Locate the red blood cells and classify each one as Plasmodium falciparum-infected, uninfected, or of indeterminate infection status.
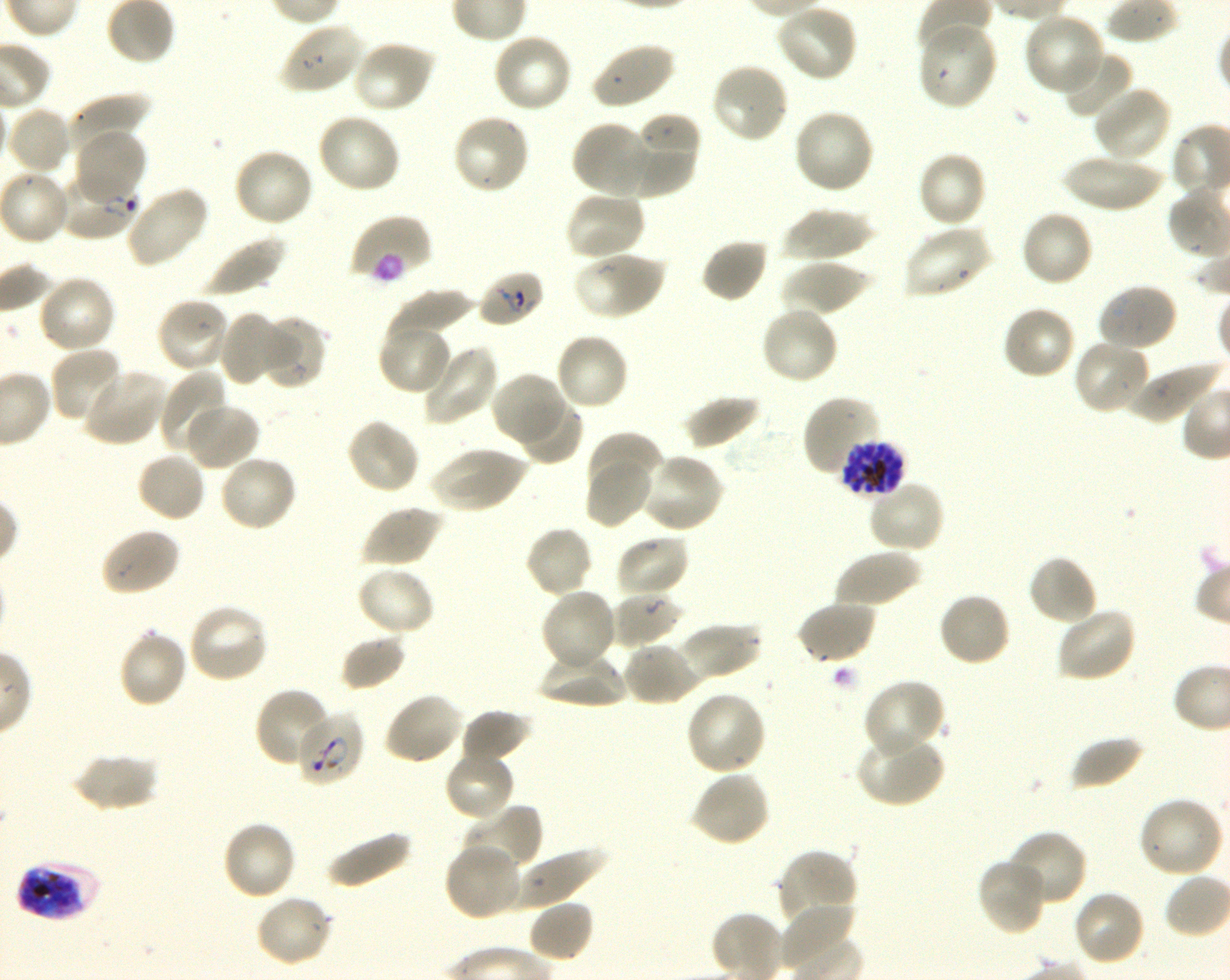

Approximate bounding boxes as (x1, y1, x2, y2) in pixels. Not every red blood cell is marked. A life-cycle stage — or a range of stages, where the recorded stages span more than one — follows each staged infected red blood cell.
Infected red blood cells: (55, 171, 140, 241) ring; (839, 439, 906, 502) schizont; (16, 858, 101, 922) late trophozoite to late schizont.
Red blood cells of indeterminate infection status: (350, 214, 433, 286), (477, 270, 546, 329), (295, 710, 363, 786).
Uninfected red blood cells: (775, 3, 859, 82), (1023, 13, 1107, 96), (280, 21, 366, 96), (917, 21, 998, 111), (491, 32, 573, 114), (352, 39, 435, 114), (590, 41, 675, 110), (1058, 47, 1133, 120), (710, 62, 789, 144), (1093, 84, 1173, 163), (68, 94, 148, 158), (6, 106, 72, 175), (792, 108, 876, 195), (316, 112, 401, 194), (450, 112, 532, 196), (637, 113, 700, 168), (570, 121, 657, 197), (623, 126, 698, 195), (75, 127, 148, 205), (233, 148, 315, 229), (916, 152, 988, 230), (1060, 154, 1165, 212), (124, 186, 208, 269), (564, 190, 646, 262), (780, 207, 874, 262), (1019, 209, 1094, 287), (902, 224, 994, 299), (200, 234, 285, 297), (700, 237, 770, 303), (572, 250, 664, 321), (779, 260, 872, 316), (35, 273, 118, 354), (1096, 283, 1179, 352), (385, 290, 475, 345), (156, 297, 231, 375), (1001, 304, 1078, 381), (758, 305, 839, 386), (219, 309, 287, 386), (261, 315, 326, 389), (377, 322, 454, 396), (554, 331, 631, 412), (1072, 339, 1151, 415), (420, 343, 500, 426), (49, 346, 125, 424), (1125, 359, 1223, 424), (82, 369, 167, 448), (161, 372, 230, 456), (490, 372, 565, 447), (682, 395, 763, 451), (802, 396, 883, 479), (514, 398, 582, 466), (182, 401, 260, 471), (345, 417, 421, 495), (587, 430, 663, 499), (429, 445, 527, 514), (135, 450, 207, 523), (640, 452, 724, 535), (218, 454, 299, 533), (585, 458, 654, 528), (866, 479, 946, 554), (362, 505, 442, 568), (524, 525, 594, 599), (100, 527, 181, 597), (615, 533, 691, 600), (833, 547, 921, 609), (1027, 554, 1098, 627), (355, 565, 436, 638), (540, 588, 618, 673), (610, 591, 683, 647), (937, 591, 1012, 668), (796, 600, 877, 665), (188, 602, 271, 684), (1056, 606, 1137, 684), (678, 622, 762, 682), (118, 628, 188, 709), (340, 634, 408, 691), (622, 640, 701, 706), (538, 649, 629, 708), (862, 680, 944, 759), (253, 688, 335, 770), (685, 690, 768, 776), (383, 691, 465, 766), (459, 709, 531, 764), (855, 733, 943, 807), (1070, 735, 1146, 791), (443, 748, 516, 821), (71, 752, 158, 811), (689, 769, 771, 847), (1137, 796, 1225, 878), (463, 803, 543, 873), (222, 819, 297, 901), (325, 828, 412, 890), (1005, 830, 1088, 909), (442, 841, 523, 922), (512, 846, 606, 909), (776, 849, 859, 931), (977, 857, 1048, 937), (1071, 888, 1147, 966), (254, 894, 335, 967), (527, 899, 595, 963), (777, 905, 861, 966).

{
  "culture": "Plasmodium falciparum strain 3D7, shaking, in vitro",
  "life_cycle_stages_observed": "ring, schizont",
  "image_size": "1230×980 pixels",
  "donor_blood_group": "O+",
  "objective": "100x, oil immersion, numerical aperture 1.30",
  "field_of_view": "single",
  "stain": "Giemsa",
  "preparation": "thin blood smear"
}